Name the parasite shown.
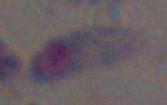
This is Toxoplasma gondii.

Micrograph. Captured at 1000x magnification.